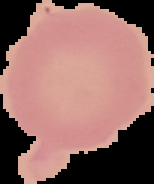
Summary:
  - Image size: 154×184 pixels
  - Image type: segmented cell region on a black background
  - Preparation: thin blood smear
  - Result: no Plasmodium parasites seen